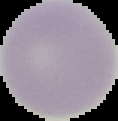 Result: no malaria parasites detected. Image is 118×121 pixels. Segmented cell region on a black background. From a thin blood film.